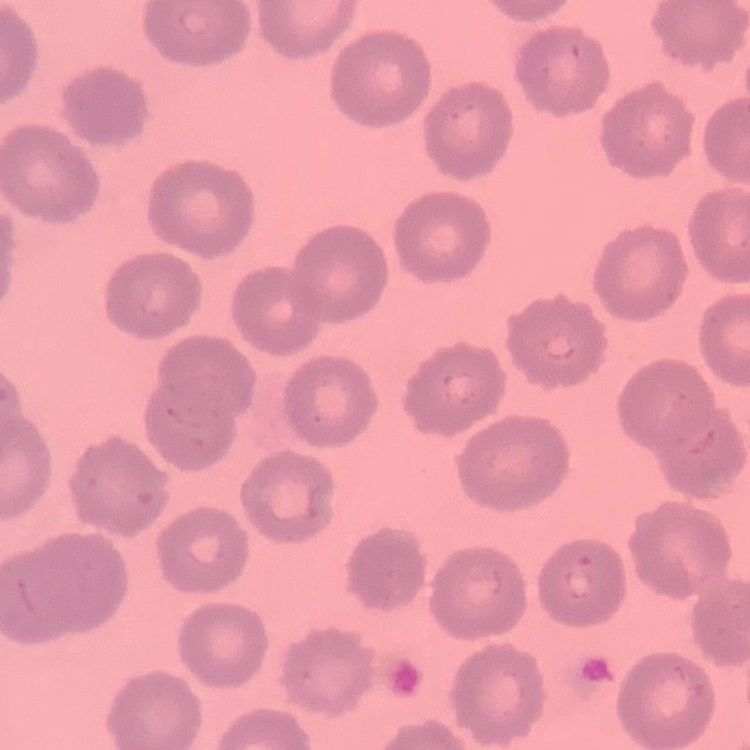

Summary:
  - Erythrocyte morphology: no rouleaux formation
  - Image type: one tile cut from a larger photomicrograph
  - Stain: Field's or Giemsa
  - Preparation: thin blood film